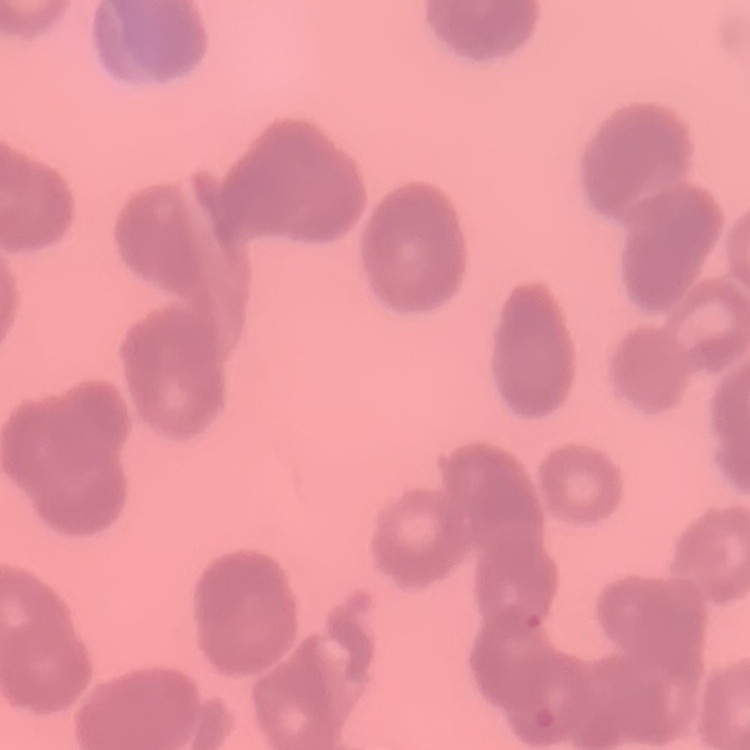

red blood cell morphology = rouleaux formation
stain = Field's or Giemsa
preparation = thin blood smear
image type = square crop of a larger photomicrograph